Classify this cell by malaria status.
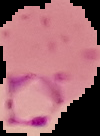

Parasitized.

Image is 100×136 pixels. Segmented cell region on a black background. From a thin blood smear.